Assess the morphology of the red blood cells.
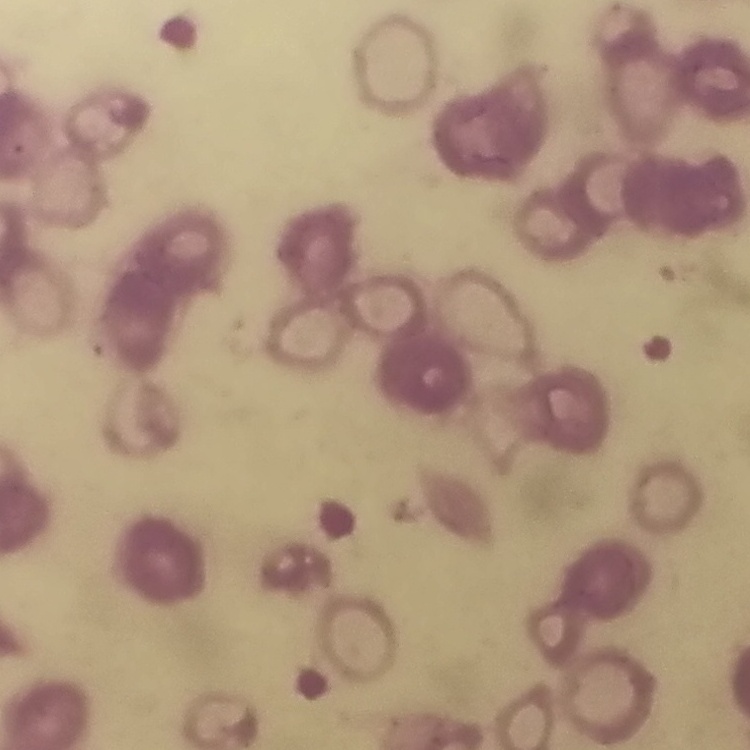
Rouleaux formation.

preparation = thin blood smear
image type = one tile cut from a larger photomicrograph
stain = Field's or Giemsa